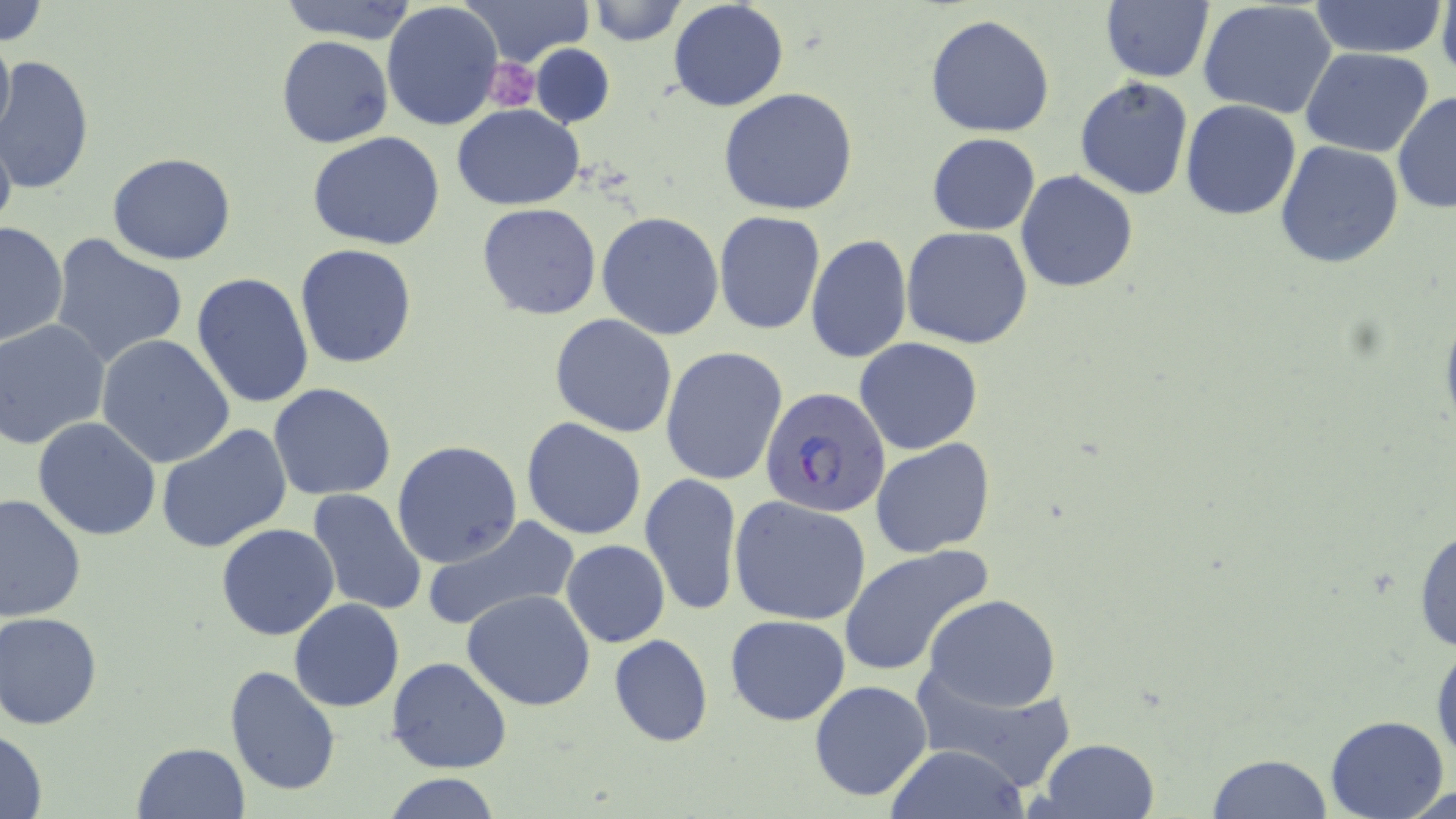
Summary:
  - Coordinate format: approximate bounding boxes as named x1/y1/x2/y2 corners in pixels
  - Plasmodium falciparum-infected red blood cell locations: (x1=761, y1=388, x2=893, y2=518)
  - Platelet locations: (x1=483, y1=56, x2=539, y2=109)
  - Uninfected red blood cell locations: (x1=0, y1=0, x2=48, y2=47), (x1=278, y1=0, x2=421, y2=43), (x1=463, y1=0, x2=593, y2=66), (x1=585, y1=0, x2=687, y2=46), (x1=1099, y1=0, x2=1214, y2=83), (x1=1438, y1=0, x2=1456, y2=81), (x1=667, y1=1, x2=789, y2=113), (x1=1196, y1=1, x2=1338, y2=118), (x1=1307, y1=1, x2=1447, y2=58), (x1=381, y1=2, x2=504, y2=133), (x1=925, y1=14, x2=1056, y2=138), (x1=0, y1=26, x2=15, y2=148), (x1=276, y1=36, x2=393, y2=149), (x1=531, y1=43, x2=614, y2=128), (x1=1301, y1=47, x2=1434, y2=158), (x1=0, y1=55, x2=94, y2=195), (x1=1074, y1=77, x2=1194, y2=201), (x1=718, y1=87, x2=859, y2=215), (x1=1391, y1=90, x2=1455, y2=215), (x1=1180, y1=99, x2=1303, y2=220), (x1=453, y1=104, x2=585, y2=210), (x1=0, y1=124, x2=17, y2=245), (x1=307, y1=132, x2=446, y2=251), (x1=927, y1=133, x2=1040, y2=235), (x1=1274, y1=140, x2=1404, y2=268), (x1=107, y1=152, x2=236, y2=265), (x1=1015, y1=169, x2=1138, y2=293), (x1=477, y1=202, x2=601, y2=319), (x1=714, y1=209, x2=825, y2=335), (x1=596, y1=211, x2=725, y2=341), (x1=0, y1=221, x2=69, y2=348), (x1=902, y1=226, x2=1034, y2=349), (x1=48, y1=234, x2=189, y2=370), (x1=806, y1=235, x2=912, y2=363), (x1=294, y1=244, x2=417, y2=368), (x1=288, y1=245, x2=411, y2=502), (x1=190, y1=272, x2=315, y2=410), (x1=549, y1=313, x2=678, y2=438), (x1=1, y1=320, x2=111, y2=451), (x1=96, y1=334, x2=238, y2=469), (x1=853, y1=338, x2=984, y2=455), (x1=659, y1=347, x2=788, y2=488), (x1=268, y1=383, x2=397, y2=500), (x1=33, y1=417, x2=161, y2=540), (x1=521, y1=417, x2=650, y2=541), (x1=156, y1=423, x2=293, y2=554), (x1=869, y1=437, x2=996, y2=559), (x1=392, y1=440, x2=524, y2=570), (x1=639, y1=472, x2=743, y2=619), (x1=306, y1=487, x2=428, y2=617), (x1=0, y1=493, x2=87, y2=626), (x1=730, y1=495, x2=874, y2=627), (x1=423, y1=515, x2=580, y2=633), (x1=1413, y1=519, x2=1456, y2=659), (x1=216, y1=522, x2=341, y2=640), (x1=561, y1=540, x2=671, y2=648), (x1=837, y1=543, x2=992, y2=677), (x1=463, y1=590, x2=597, y2=711), (x1=922, y1=594, x2=1061, y2=711), (x1=289, y1=599, x2=405, y2=712), (x1=0, y1=612, x2=104, y2=729), (x1=724, y1=614, x2=851, y2=725), (x1=608, y1=634, x2=714, y2=747), (x1=1432, y1=636, x2=1456, y2=773), (x1=387, y1=656, x2=512, y2=773), (x1=224, y1=664, x2=341, y2=797), (x1=913, y1=666, x2=1073, y2=792), (x1=807, y1=679, x2=935, y2=802), (x1=1323, y1=714, x2=1451, y2=819), (x1=0, y1=728, x2=49, y2=817), (x1=1033, y1=738, x2=1163, y2=819), (x1=131, y1=742, x2=252, y2=818), (x1=882, y1=745, x2=1029, y2=819), (x1=1203, y1=753, x2=1336, y2=818), (x1=384, y1=773, x2=503, y2=819)
  - Slide-level diagnosis: Plasmodium falciparum
  - Magnification: 1000x
  - Preparation: thin blood smear
  - Modality: optical microscopy
  - Image size: 1456×819 pixels
  - Stain: May-Grünwald-Giemsa
  - Field of view: single